Give the preparation type.
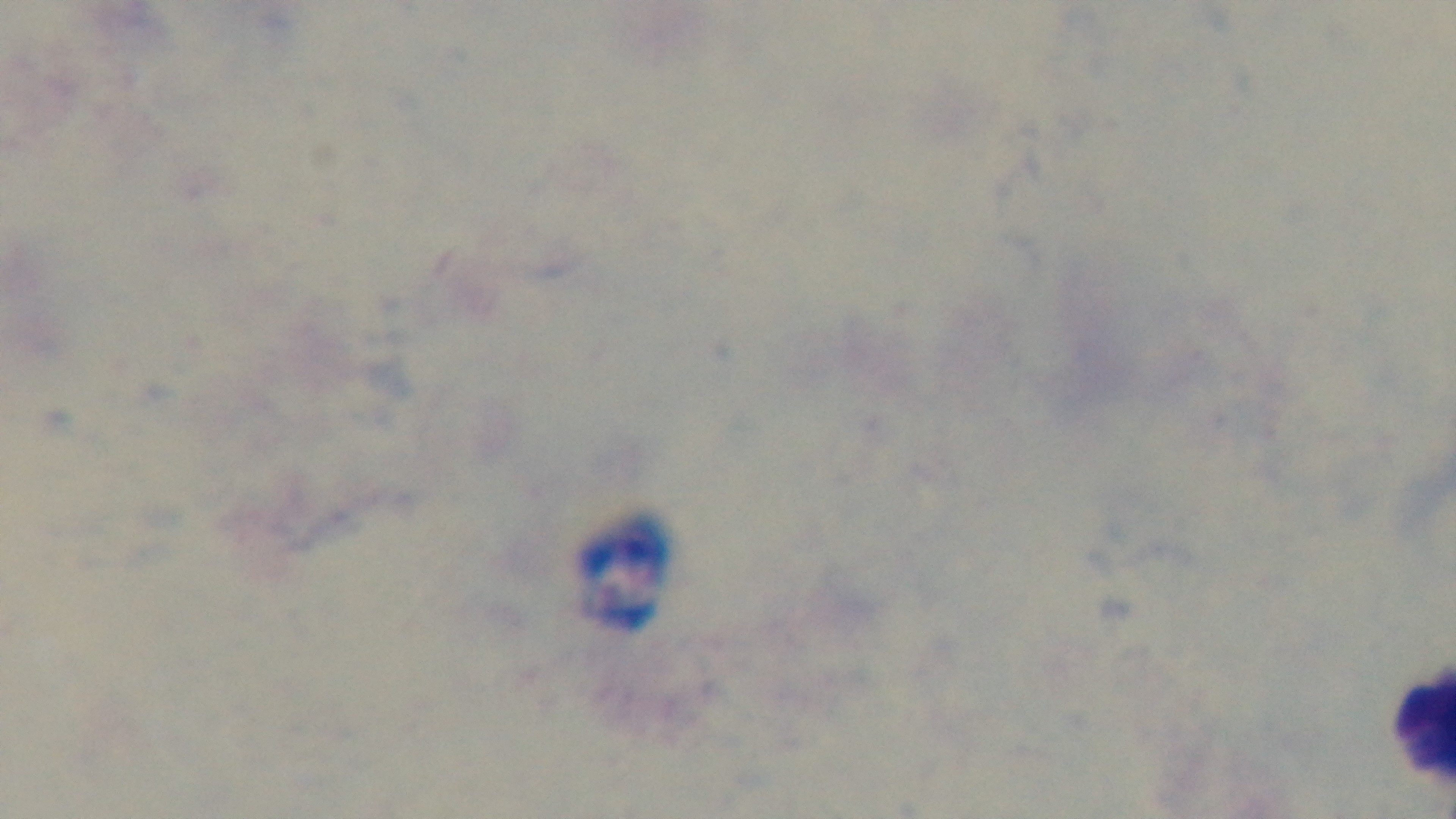
It is a thick blood film.

modality = light microscopy
capture = mounted 4K digital camera
objective = 100x oil immersion
stain = Giemsa
malaria status = negative
field of view = single